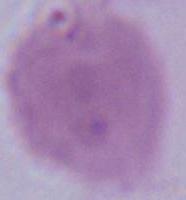 1000x magnification. A red blood cell is seen. Photomicrograph.